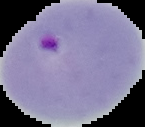
Summary:
  - Preparation: thin blood smear
  - Image size: 145×127 pixels
  - Result: Plasmodium parasites identified
  - Image type: segmented cell region on a black background